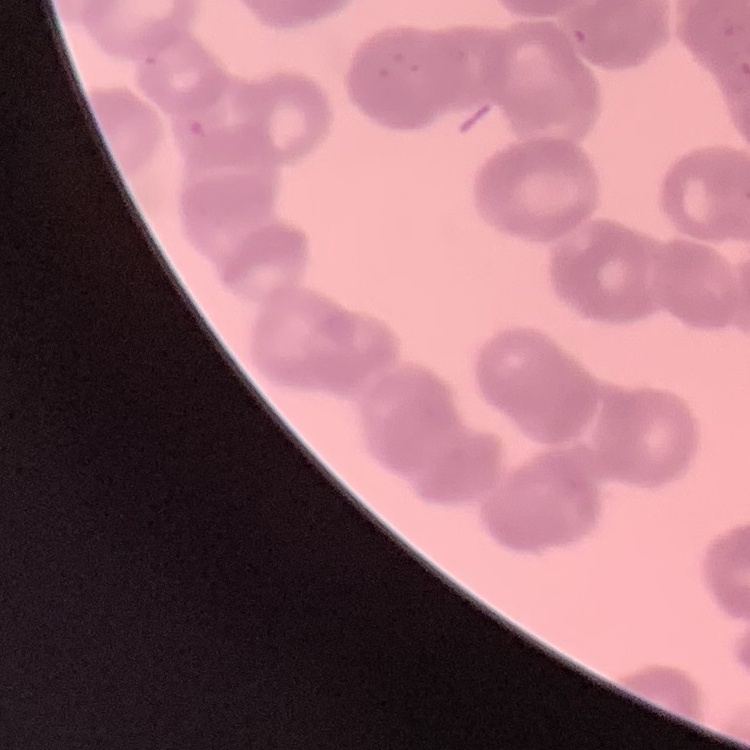

erythrocyte morphology = rouleaux formation
stain = Field's or Giemsa
preparation = thin blood film
image type = square crop of a larger photomicrograph